Evaluate for parasitized red blood cells.
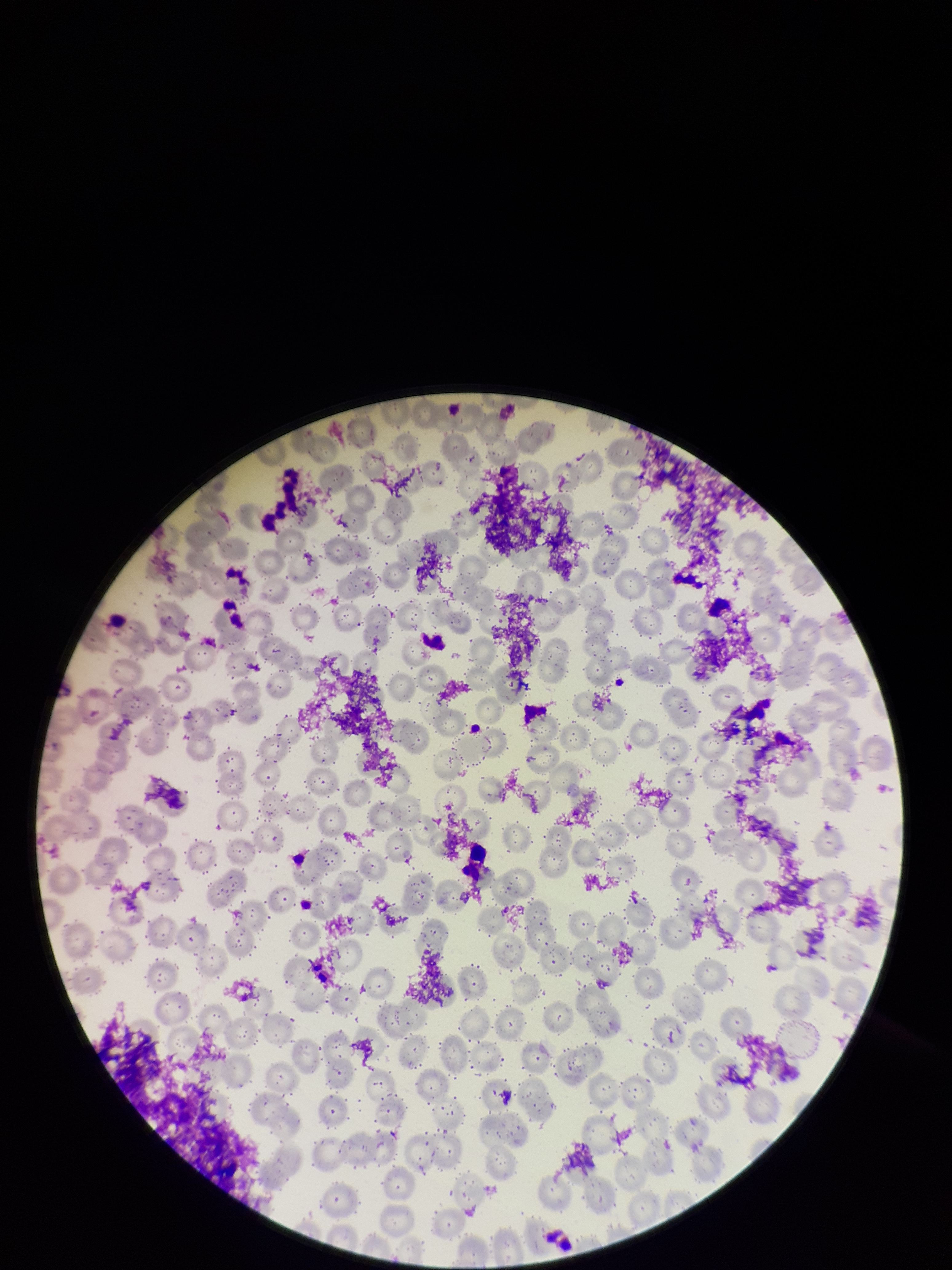
None detected.

patient_malaria_status: negative
stain: Giemsa
capture: smartphone photograph through the microscope eyepiece
parasitized_red_blood_cell_count: 0
preparation: thin blood smear
field_of_view: single
image_size: 952×1270 pixels
red_blood_cell_count: 281